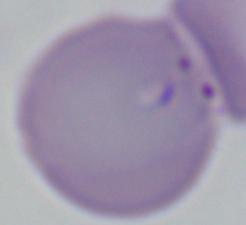
A Babesia parasite is seen. Captured at 1000x magnification. Micrograph.